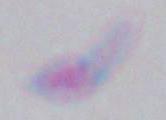

modality = photomicrograph
magnification = 1000x
identification = Toxoplasma gondii